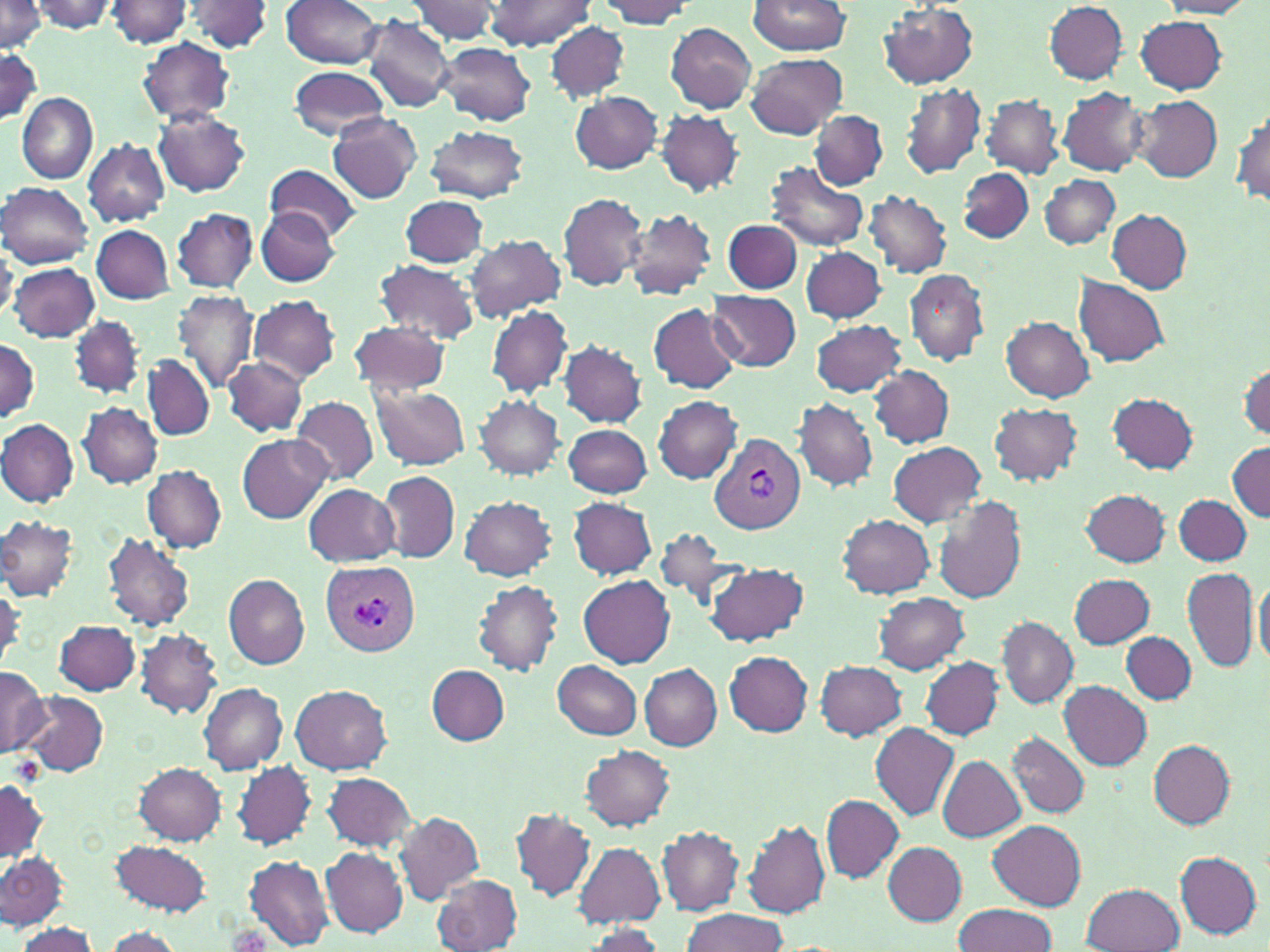

Approximate bounding boxes as (x1, y1, x2, y2) in pixels. Uninfected red blood cell locations: (31, 0, 120, 33), (105, 0, 194, 48), (280, 0, 385, 68), (405, 0, 505, 46), (490, 0, 597, 50), (594, 0, 695, 29), (0, 1, 48, 54), (180, 1, 277, 54), (747, 1, 852, 57), (1156, 1, 1254, 17), (1043, 2, 1130, 82), (879, 4, 979, 89), (360, 15, 454, 113), (1135, 15, 1226, 94), (665, 22, 756, 114), (545, 23, 630, 103), (138, 36, 235, 125), (435, 42, 536, 126), (0, 50, 43, 123), (1, 50, 42, 124), (746, 53, 847, 138), (288, 67, 391, 139), (900, 82, 987, 179), (1058, 88, 1147, 176), (17, 91, 97, 184), (569, 91, 662, 174), (981, 94, 1063, 178), (1131, 94, 1222, 182), (1232, 108, 1269, 209), (152, 109, 250, 197), (657, 109, 744, 197), (809, 109, 888, 189), (328, 112, 421, 204), (424, 125, 528, 203), (82, 139, 170, 228), (768, 160, 868, 251), (267, 164, 361, 241), (959, 167, 1033, 243), (1041, 176, 1121, 248), (0, 182, 94, 269), (865, 189, 952, 278), (558, 190, 648, 291), (402, 195, 490, 267), (257, 207, 339, 286), (172, 208, 258, 292), (1107, 208, 1192, 293), (624, 209, 718, 301), (724, 219, 801, 293), (92, 225, 174, 303), (464, 233, 565, 323), (0, 240, 19, 322), (801, 247, 887, 323), (373, 259, 480, 344), (8, 261, 98, 342), (906, 269, 988, 367), (1074, 277, 1169, 368), (707, 288, 801, 371), (172, 290, 258, 394), (247, 294, 340, 383), (648, 304, 739, 394), (486, 306, 573, 398), (69, 315, 146, 397), (1001, 317, 1094, 401), (810, 319, 908, 397), (348, 320, 451, 394), (0, 338, 40, 422), (556, 339, 646, 425), (144, 354, 214, 441), (221, 356, 308, 436), (1240, 363, 1270, 440), (868, 364, 954, 449), (369, 384, 469, 471), (1107, 392, 1199, 474), (474, 396, 566, 480), (652, 396, 741, 482), (292, 397, 378, 483), (793, 397, 878, 492), (989, 402, 1082, 486), (77, 403, 162, 488), (0, 420, 78, 507), (563, 423, 652, 498), (237, 434, 333, 523), (889, 442, 987, 526), (1228, 442, 1269, 521), (141, 466, 226, 553), (378, 470, 460, 564), (303, 483, 399, 567), (1081, 489, 1169, 567), (932, 494, 1027, 605), (1173, 494, 1251, 566), (459, 495, 558, 580), (568, 497, 656, 579), (840, 514, 935, 597), (0, 515, 79, 601), (653, 528, 736, 610), (103, 531, 196, 632), (705, 561, 809, 646), (1182, 567, 1259, 673), (579, 574, 676, 670), (1068, 574, 1157, 648), (1254, 574, 1270, 667), (222, 575, 310, 669), (472, 579, 562, 676), (875, 593, 970, 674), (997, 616, 1079, 708), (55, 619, 141, 695), (135, 628, 223, 719), (1122, 632, 1195, 704), (724, 651, 813, 736), (919, 656, 1003, 740), (553, 661, 642, 738), (815, 661, 908, 740), (426, 664, 509, 745), (638, 664, 722, 750), (0, 665, 50, 757), (1060, 680, 1152, 770), (199, 682, 288, 774), (291, 684, 393, 773), (21, 692, 109, 775), (871, 722, 960, 820), (1008, 731, 1089, 819), (1149, 740, 1236, 828), (581, 746, 675, 830), (937, 757, 1023, 841), (232, 761, 316, 851), (135, 762, 226, 844), (323, 772, 416, 851), (0, 778, 48, 863), (820, 795, 903, 882), (510, 809, 595, 901), (393, 811, 484, 905), (742, 817, 830, 919), (990, 821, 1085, 909), (657, 826, 744, 915), (110, 839, 211, 918), (883, 842, 967, 925), (574, 843, 665, 927), (321, 847, 407, 937), (0, 851, 67, 929), (1174, 851, 1262, 939), (246, 854, 334, 950), (431, 874, 523, 952), (1082, 882, 1184, 952), (953, 903, 1056, 952), (680, 909, 788, 951), (17, 923, 101, 951), (576, 925, 667, 951), (102, 927, 184, 950). Plasmodium vivax-infected red blood cell locations: (710, 434, 806, 534), (321, 562, 420, 657). Slide-level diagnosis: Plasmodium vivax. 1000x magnification. One field of a larger specimen. Light microscopy. May-Grünwald-Giemsa-stained preparation. Thin blood film. Image is 1270×952 pixels.